Classify the preparation.
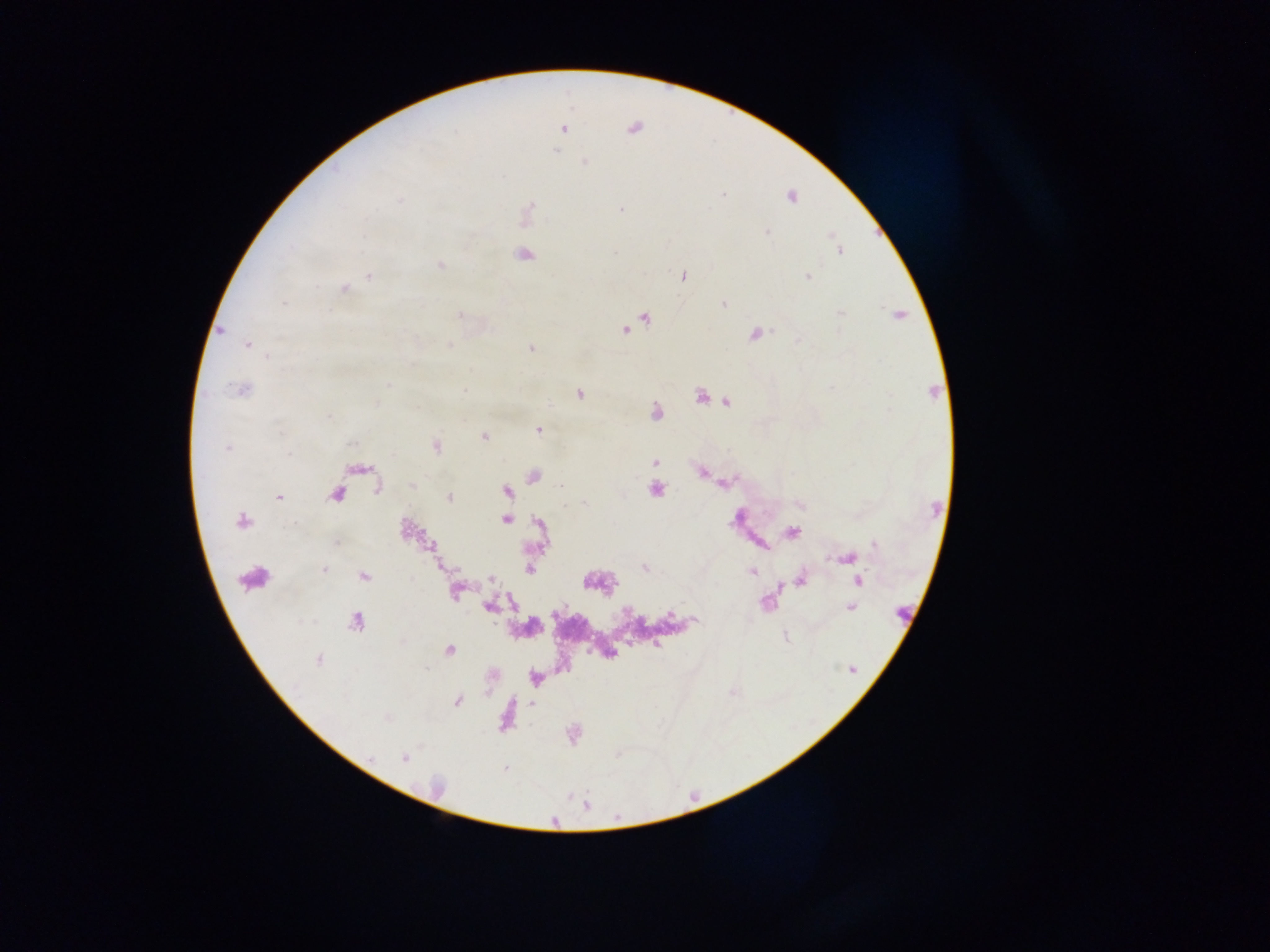
Thick blood film.

Approximate centers as [x, y] in pixels. Plasmodium parasite locations: [634, 128], [563, 129], [555, 151], [585, 162], [724, 195], [791, 197], [400, 199], [529, 208], [620, 209], [767, 232], [830, 235], [364, 237], [840, 250], [615, 252], [523, 255], [440, 264], [369, 276], [683, 277], [807, 277], [344, 288], [284, 302], [723, 304], [840, 313], [459, 314], [898, 315], [646, 318], [626, 330], [221, 331], [755, 334], [798, 340], [247, 345], [449, 346], [531, 349], [268, 356], [389, 384], [831, 388], [241, 389], [464, 390], [580, 393], [700, 397], [727, 402], [376, 404], [654, 411], [330, 418], [538, 430], [484, 436], [352, 444], [436, 446], [227, 448], [289, 453], [654, 462], [701, 472], [533, 476], [727, 482], [412, 485], [561, 487], [656, 489], [506, 491], [336, 493], [279, 497], [449, 497], [583, 504], [800, 505], [505, 520], [241, 521], [793, 532], [336, 543], [875, 544], [847, 559], [645, 568], [324, 570], [530, 570], [751, 571], [364, 575], [490, 579], [801, 579], [859, 580], [455, 592], [766, 602], [490, 607], [851, 608], [670, 614], [696, 620], [355, 622], [657, 645], [449, 650], [318, 659], [426, 668], [853, 669], [457, 701], [404, 757], [505, 768]. Sample from Ghana. Image is 1270×952 pixels. Single field of view. Photographed through a microscope with a mobile-phone camera.